State which parasite is depicted.
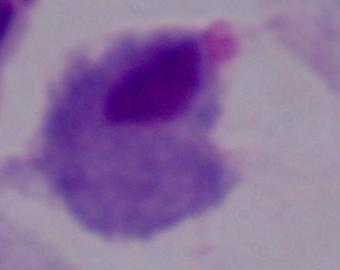

A trichomonad.

Summary:
  - Modality: micrograph
  - Magnification: 1000x